Point out each leukocyte.
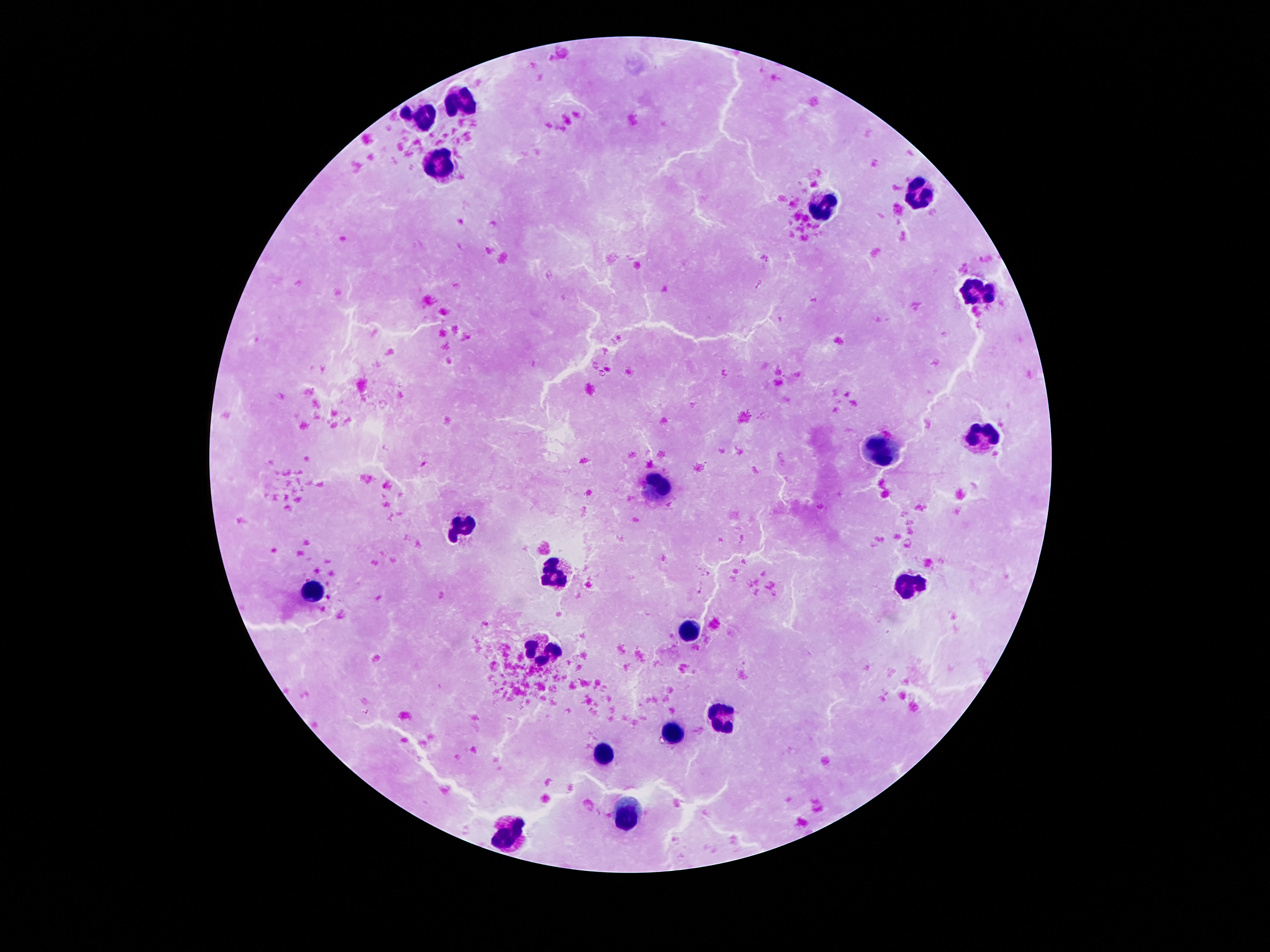

Approximate centers as [x, y] in pixels.
Leukocytes: [460, 100], [422, 115], [438, 163], [923, 194], [823, 208], [975, 293], [980, 435], [881, 452], [656, 488], [464, 527], [557, 573], [909, 588], [315, 591], [691, 631], [543, 654], [718, 718], [674, 733], [604, 753], [625, 813], [509, 835].

Patient malaria status: negative. Image is 1270×952 pixels. Smartphone photograph taken through the microscope eyepiece. 100x magnification. Giemsa-stained preparation. Single field of view. Thick blood smear.